Outline each blood parasite and name the species.
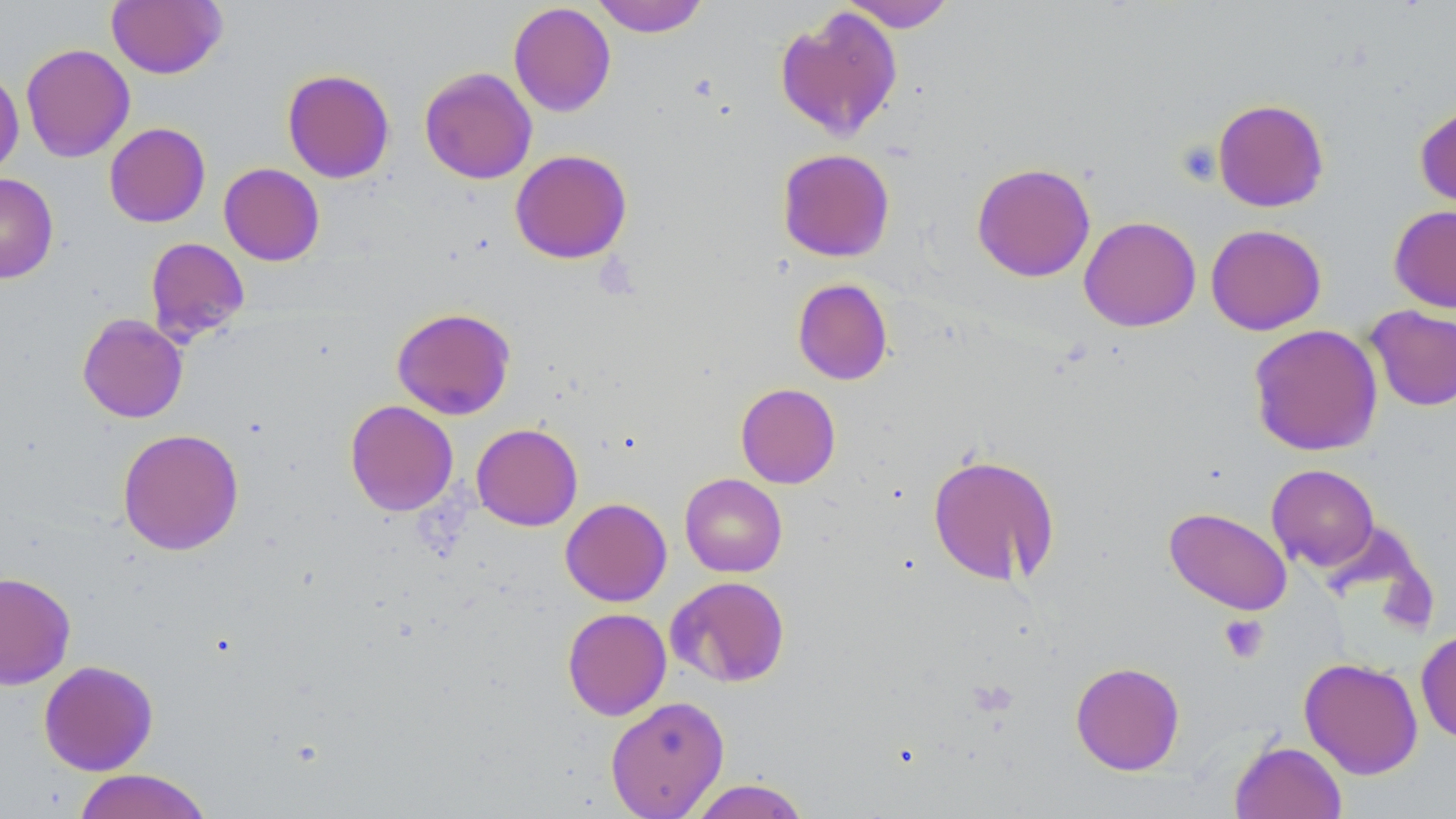

No blood parasites observed.

Approximate bounding boxes as (x1,y1)-(x2,y2) corner pairs in pixels. Platelet locations: (1176,141)-(1222,185), (1218,613)-(1269,663). Uninfected red blood cell locations: (106,0)-(227,79), (591,0)-(709,37), (839,1)-(956,32), (508,3)-(616,117), (774,5)-(903,142), (20,43)-(135,162), (419,67)-(537,184), (282,68)-(395,183), (0,69)-(24,179), (1212,98)-(1329,212), (1414,101)-(1456,215), (104,122)-(211,227), (777,148)-(895,262), (509,149)-(632,264), (218,162)-(325,266), (971,162)-(1096,282), (0,173)-(58,284), (1389,204)-(1456,313), (1079,216)-(1201,332), (1205,224)-(1326,335), (145,237)-(250,345), (792,278)-(893,385), (1364,305)-(1456,411), (391,307)-(516,420), (77,313)-(188,423), (1248,323)-(1383,456), (735,383)-(841,489), (345,400)-(458,516), (471,423)-(582,531), (117,427)-(244,556), (927,453)-(1060,586), (1266,464)-(1379,571), (679,473)-(788,577), (560,497)-(671,606), (1164,507)-(1293,615), (0,571)-(76,689), (666,575)-(791,688), (562,607)-(672,720), (1415,627)-(1456,743), (1299,657)-(1423,779), (38,660)-(159,776), (1070,661)-(1186,776), (605,696)-(729,817), (1230,740)-(1347,819), (72,769)-(214,819), (687,779)-(811,818). Slide-level diagnosis: negative for blood parasites. Thin blood film. 1000x magnification. Image is 1456×819 pixels. Single field of view. Light microscopy. May-Grünwald-Giemsa-stained preparation.